Locate every blood parasite and identify its species.
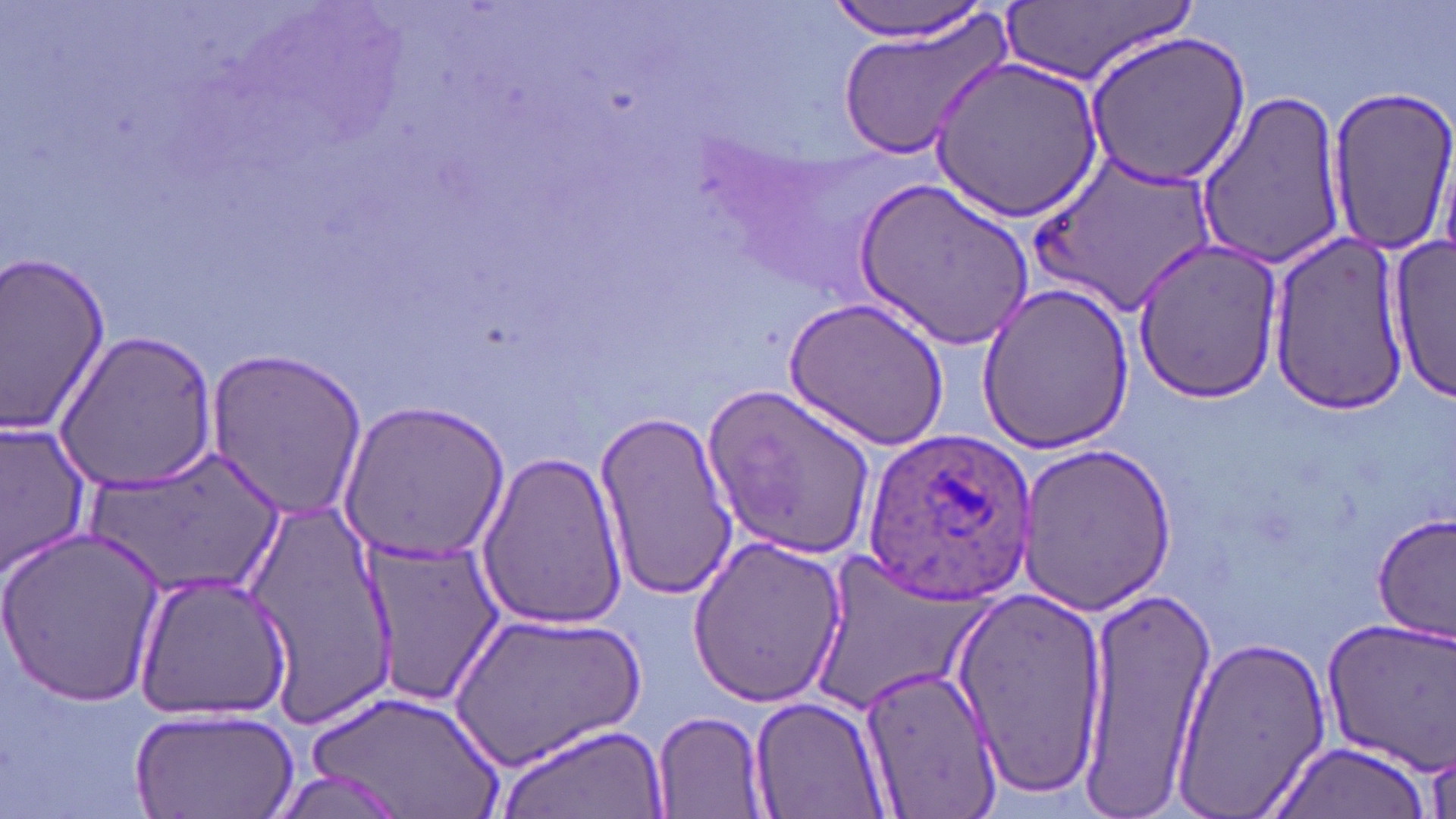
Approximate bounding boxes as [x1, y1, x2, y2] in pixels.
Plasmodium ovale-infected red blood cells: [862, 429, 1037, 604].
No Plasmodium falciparum, Plasmodium malariae, Plasmodium vivax, Babesia divergens, or Trypanosoma brucei observed.

Uninfected red blood cell locations: [825, 0, 998, 44], [1000, 0, 1193, 90], [833, 12, 1014, 161], [1082, 29, 1252, 189], [930, 56, 1105, 224], [1324, 85, 1456, 258], [1194, 88, 1347, 269], [1036, 153, 1218, 315], [857, 180, 1034, 350], [1267, 230, 1412, 416], [1385, 240, 1455, 404], [1131, 241, 1286, 404], [0, 248, 114, 442], [974, 280, 1135, 453], [785, 295, 950, 452], [54, 328, 220, 494], [202, 350, 371, 521], [702, 387, 878, 558], [337, 400, 508, 567], [592, 409, 739, 599], [0, 419, 95, 578], [1015, 442, 1180, 613], [85, 445, 289, 604], [473, 449, 630, 630], [243, 493, 401, 724], [1372, 510, 1454, 642], [0, 527, 166, 704], [685, 534, 848, 706], [360, 538, 503, 706], [803, 553, 992, 719], [134, 568, 293, 722], [947, 582, 1107, 797], [1073, 584, 1212, 803], [444, 609, 648, 771], [1319, 617, 1456, 773], [1171, 633, 1334, 816], [858, 663, 999, 813], [302, 689, 508, 818], [748, 694, 890, 818], [651, 708, 771, 817], [129, 710, 299, 819], [492, 723, 671, 819], [1266, 740, 1434, 819]. Slide-level diagnosis: Plasmodium ovale. Single field of view. Thin blood film. Image is 1456×819 pixels. 1000x magnification. May-Grünwald-Giemsa-stained preparation. Optical microscopy.